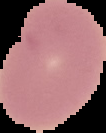

result = negative for Plasmodium parasites
image size = 106×133 pixels
image type = cell region segmented out of the field of view; surrounding area masked to black
preparation = thin blood film